Assess this cell for malaria.
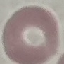
Uninfected.

Summary:
  - Capture: smartphone through the microscope eyepiece
  - Stain: Giemsa
  - Image type: cell patch, automatically extracted from a larger field of view and resized to 64 × 64 pixels
  - Preparation: thin smear